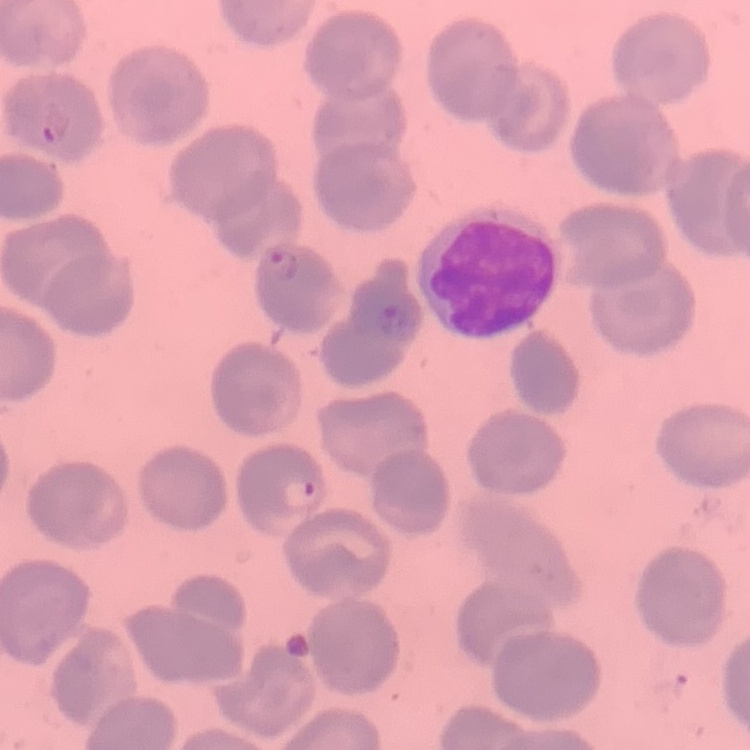

{
  "erythrocyte_morphology": "no rouleaux formation",
  "preparation": "thin blood film",
  "stain": "Field's or Giemsa",
  "image_type": "one tile cut from a larger photomicrograph"
}